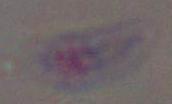 Photomicrograph. Toxoplasma gondii is shown. Captured at 1000x magnification.